Mark where platelets are.
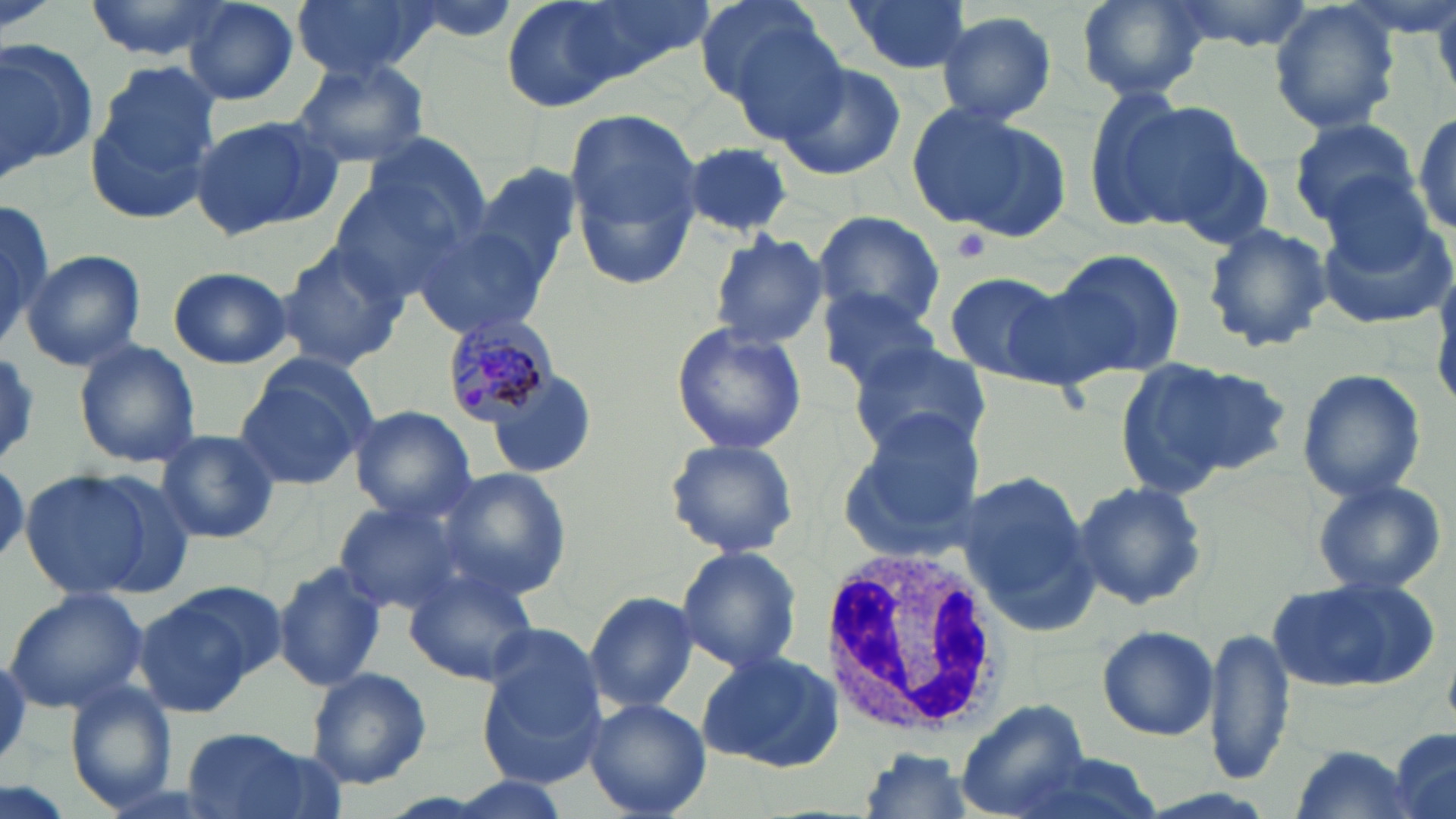

Approximate bounding boxes as named x1/y1/x2/y2 corners in pixels.
Platelets: (x1=949, y1=228, x2=991, y2=264).

Summary:
  - White blood cell locations: (x1=822, y1=544, x2=1005, y2=738)
  - Uninfected red blood cell locations: (x1=82, y1=0, x2=234, y2=60), (x1=292, y1=0, x2=437, y2=79), (x1=498, y1=0, x2=661, y2=112), (x1=574, y1=0, x2=713, y2=76), (x1=692, y1=0, x2=839, y2=121), (x1=842, y1=0, x2=972, y2=75), (x1=1073, y1=0, x2=1210, y2=99), (x1=1163, y1=0, x2=1317, y2=50), (x1=182, y1=2, x2=301, y2=106), (x1=1269, y1=2, x2=1404, y2=135), (x1=933, y1=10, x2=1058, y2=126), (x1=0, y1=39, x2=97, y2=175), (x1=290, y1=57, x2=432, y2=170), (x1=774, y1=58, x2=908, y2=181), (x1=85, y1=64, x2=221, y2=223), (x1=1099, y1=97, x2=1253, y2=232), (x1=904, y1=102, x2=1067, y2=238), (x1=563, y1=108, x2=702, y2=292), (x1=1410, y1=110, x2=1454, y2=238), (x1=187, y1=114, x2=337, y2=239), (x1=1286, y1=115, x2=1420, y2=226), (x1=682, y1=141, x2=795, y2=238), (x1=1165, y1=141, x2=1277, y2=252), (x1=468, y1=164, x2=583, y2=292), (x1=325, y1=167, x2=478, y2=303), (x1=1317, y1=173, x2=1438, y2=273), (x1=0, y1=195, x2=52, y2=350), (x1=809, y1=211, x2=947, y2=330), (x1=1318, y1=213, x2=1454, y2=330), (x1=413, y1=223, x2=555, y2=341), (x1=1202, y1=223, x2=1332, y2=353), (x1=708, y1=231, x2=829, y2=350), (x1=275, y1=244, x2=407, y2=371), (x1=1044, y1=248, x2=1185, y2=381), (x1=21, y1=249, x2=146, y2=370), (x1=167, y1=267, x2=293, y2=368), (x1=942, y1=270, x2=1071, y2=382), (x1=815, y1=288, x2=947, y2=392), (x1=668, y1=321, x2=808, y2=455), (x1=73, y1=339, x2=201, y2=468), (x1=847, y1=339, x2=990, y2=457), (x1=0, y1=353, x2=44, y2=468), (x1=1113, y1=354, x2=1288, y2=494), (x1=233, y1=358, x2=376, y2=488), (x1=1296, y1=367, x2=1425, y2=505), (x1=490, y1=373, x2=595, y2=478), (x1=349, y1=405, x2=476, y2=520), (x1=835, y1=408, x2=988, y2=564), (x1=154, y1=428, x2=281, y2=543), (x1=663, y1=437, x2=800, y2=559), (x1=434, y1=466, x2=571, y2=598), (x1=19, y1=468, x2=166, y2=603), (x1=956, y1=470, x2=1098, y2=629), (x1=1309, y1=475, x2=1451, y2=598), (x1=1071, y1=480, x2=1208, y2=612), (x1=332, y1=495, x2=476, y2=613), (x1=675, y1=546, x2=802, y2=678), (x1=272, y1=561, x2=387, y2=695), (x1=403, y1=566, x2=538, y2=688), (x1=1268, y1=574, x2=1437, y2=696), (x1=3, y1=587, x2=150, y2=715), (x1=133, y1=587, x2=270, y2=718), (x1=583, y1=590, x2=699, y2=714), (x1=1097, y1=623, x2=1218, y2=741), (x1=1208, y1=627, x2=1294, y2=784), (x1=477, y1=640, x2=608, y2=788), (x1=695, y1=647, x2=842, y2=771), (x1=304, y1=666, x2=432, y2=789), (x1=64, y1=683, x2=176, y2=810), (x1=584, y1=697, x2=711, y2=818), (x1=955, y1=700, x2=1095, y2=816), (x1=177, y1=728, x2=325, y2=819), (x1=1387, y1=728, x2=1455, y2=819), (x1=1283, y1=743, x2=1422, y2=819), (x1=855, y1=749, x2=977, y2=818), (x1=1008, y1=755, x2=1162, y2=819), (x1=436, y1=774, x2=576, y2=818)
  - Plasmodium malariae-infected red blood cell locations: (x1=441, y1=319, x2=557, y2=426)
  - Slide-level diagnosis: Plasmodium malariae
  - Modality: optical microscopy
  - Preparation: thin blood smear
  - Image size: 1456×819 pixels
  - Stain: May-Grünwald-Giemsa
  - Magnification: 1000x
  - Field of view: single